Report the malaria status of this cell.
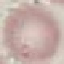

It is uninfected.

Summary:
  - Preparation: thin smear
  - Capture: smartphone camera at the microscope eyepiece
  - Image type: cell patch, automatically extracted from a larger field of view and resized to 64 × 64 pixels
  - Stain: Giemsa